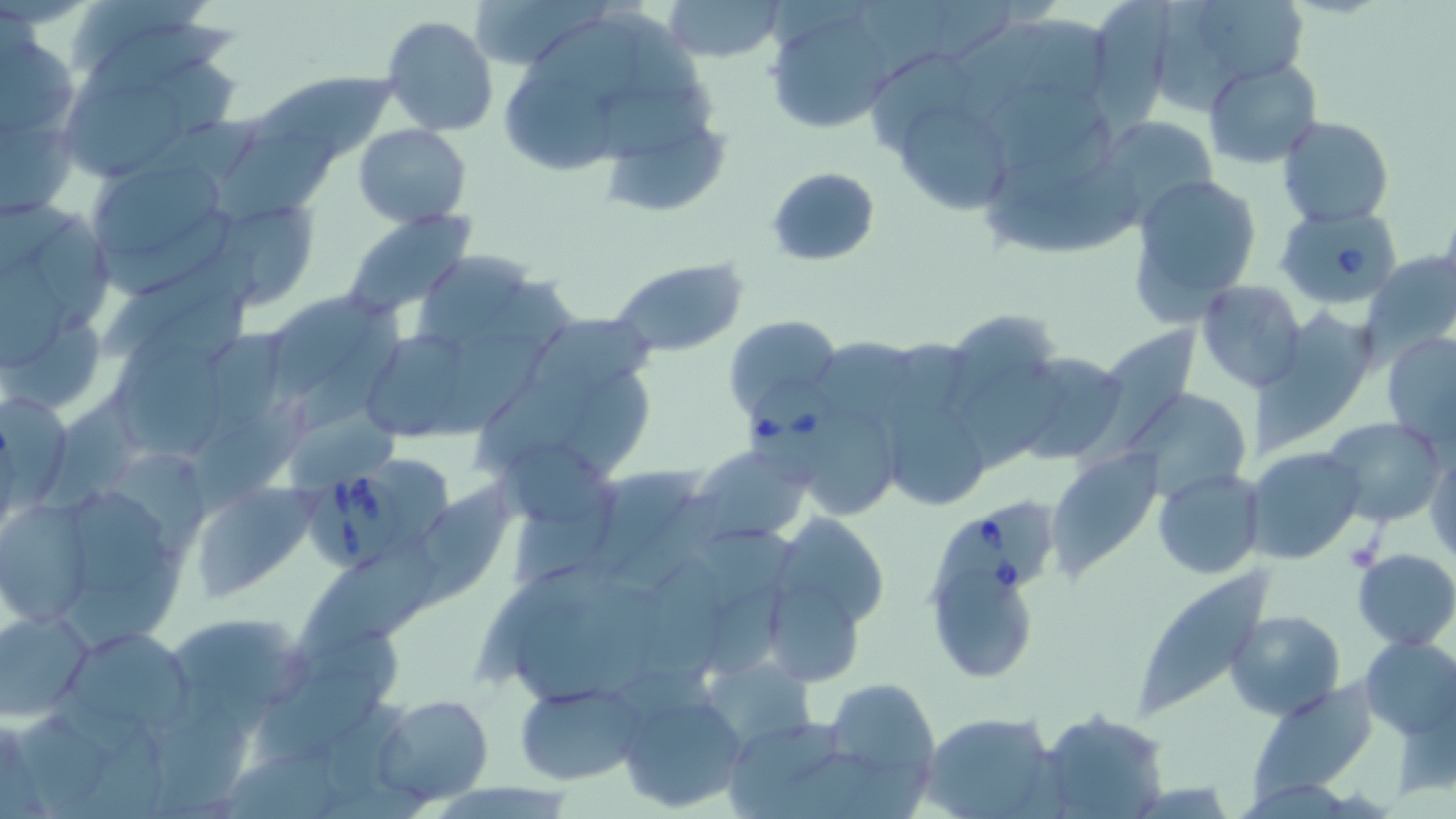 Approximate bounding boxes as [x1, y1, x2, y2] in pixels. Babesia divergens-infected red blood cell locations: [1275, 205, 1396, 306], [739, 375, 845, 487], [311, 470, 412, 573], [922, 491, 1058, 611]. Uninfected red blood cell locations: [465, 0, 596, 71], [659, 0, 787, 64], [860, 0, 956, 59], [1095, 0, 1168, 135], [1155, 1, 1245, 113], [1203, 1, 1314, 80], [762, 10, 897, 134], [620, 12, 709, 101], [1026, 14, 1116, 99], [381, 15, 499, 137], [74, 19, 240, 110], [521, 20, 644, 103], [951, 20, 1051, 122], [2, 41, 81, 140], [863, 53, 973, 154], [1205, 59, 1321, 168], [255, 71, 411, 149], [500, 75, 617, 180], [599, 83, 719, 163], [65, 84, 192, 174], [990, 88, 1111, 162], [901, 99, 1006, 213], [137, 113, 270, 200], [1096, 114, 1217, 221], [1279, 116, 1394, 226], [603, 122, 734, 212], [3, 123, 79, 212], [352, 124, 473, 226], [217, 127, 343, 226], [85, 159, 231, 286], [979, 162, 1140, 262], [766, 166, 880, 267], [1126, 171, 1262, 321], [192, 195, 324, 311], [339, 209, 478, 318], [94, 213, 235, 260], [39, 214, 116, 338], [423, 246, 526, 347], [1365, 251, 1456, 353], [608, 258, 749, 359], [5, 259, 70, 369], [475, 279, 575, 355], [1195, 280, 1307, 392], [261, 286, 389, 411], [119, 290, 249, 398], [1254, 312, 1386, 452], [723, 315, 843, 426], [5, 316, 103, 405], [525, 316, 660, 393], [949, 316, 1057, 410], [300, 319, 405, 432], [1077, 324, 1202, 477], [372, 327, 465, 439], [209, 329, 288, 426], [1381, 329, 1456, 453], [448, 333, 550, 430], [886, 335, 971, 415], [817, 338, 917, 416], [119, 344, 230, 461], [1005, 352, 1132, 466], [562, 356, 653, 479], [475, 379, 593, 478], [878, 383, 997, 515], [1131, 388, 1254, 503], [49, 389, 155, 514], [0, 393, 77, 505], [189, 404, 313, 510], [290, 407, 401, 492], [819, 407, 898, 524], [1323, 416, 1447, 526], [488, 442, 618, 525], [691, 444, 809, 543], [1245, 447, 1366, 564], [1426, 447, 1455, 565], [119, 449, 212, 557], [1048, 450, 1164, 576], [379, 455, 455, 549], [588, 463, 700, 578], [1154, 468, 1265, 580], [422, 479, 518, 603], [73, 482, 175, 603], [188, 482, 313, 602], [616, 492, 722, 586], [1, 497, 95, 629], [775, 514, 888, 622], [699, 527, 798, 608], [291, 539, 446, 663], [1352, 548, 1456, 651], [65, 561, 184, 651], [477, 562, 607, 682], [638, 562, 725, 690], [1128, 565, 1270, 722], [931, 569, 1041, 680], [579, 581, 672, 692], [713, 585, 791, 677], [773, 587, 864, 680], [0, 607, 95, 722], [505, 607, 616, 711], [1224, 609, 1345, 720], [175, 621, 318, 700], [68, 630, 202, 731], [300, 630, 406, 691], [1358, 636, 1455, 739], [699, 652, 816, 755], [251, 673, 384, 770], [821, 677, 941, 797], [514, 684, 640, 785], [616, 688, 748, 814], [372, 694, 495, 808], [157, 710, 249, 813], [919, 710, 1061, 819], [1036, 710, 1169, 818], [722, 715, 853, 815], [20, 719, 111, 811], [66, 740, 174, 819], [225, 753, 341, 819]. Slide-level diagnosis: Babesia divergens. May-Grünwald-Giemsa stain. Captured at 1000x magnification. Optical microscopy. Thin blood smear. Image is 1456×819 pixels. Single field of view.